Report the malaria status of this cell.
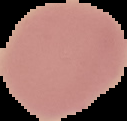

It is uninfected.

The area outside the segmented cell region is set to black. From a thin blood film. Image is 127×121 pixels.